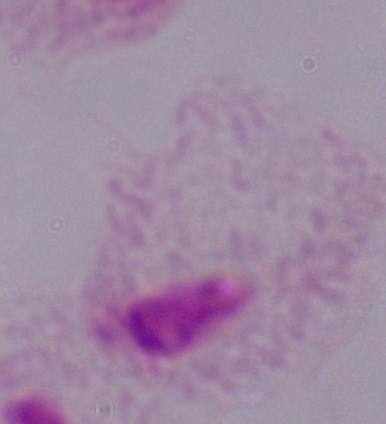
Summary:
  - Magnification: 1000x
  - Identification: trichomonad
  - Modality: photomicrograph